Classify this cell by malaria status.
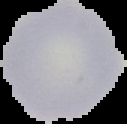
Uninfected.

image size = 127×124 pixels
image type = segmented cell region on a black background
preparation = thin blood film